Name the parasite shown.
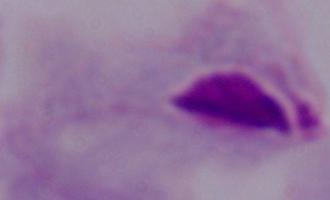

This is a trichomonad.

Captured at 1000x magnification. Photomicrograph.